Name the cell type shown.
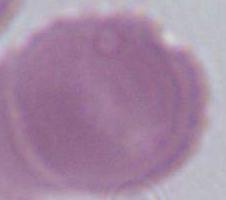
An erythrocyte.

Micrograph. 1000x magnification.